Classify this cell by malaria status.
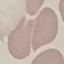
It is uninfected.

Acquired by smartphone through the microscope eyepiece. Automatically extracted cell patch, resized to 64 × 64 pixels. Thin blood film. Giemsa stain.